Classify this cell by malaria status.
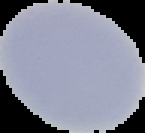

Uninfected.

Summary:
  - Image size: 145×133 pixels
  - Preparation: thin blood film
  - Image type: segmented cell region with the area outside set to black